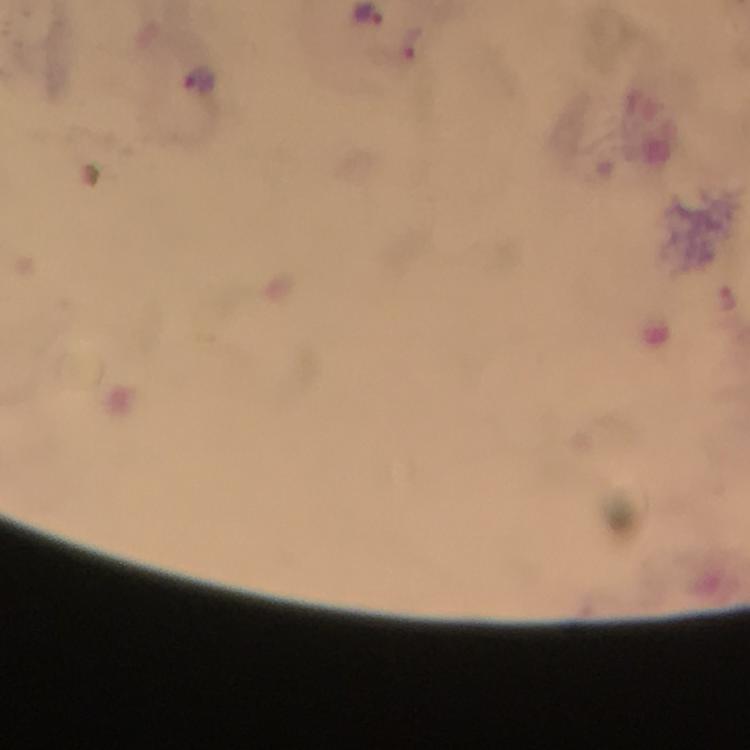
Approximate centers as {x, y} in pixels. Malaria parasite locations: {371, 16}, {413, 44}, {198, 78}, {729, 297}. Immersion oil applied. From a malaria diagnostic workup. Photographed through the microscope with a smartphone camera. Image is 750×750 pixels. Thick smear. 100x magnification. Giemsa-stained preparation. Cropped region of a single field of view.